Assess this cell for malaria.
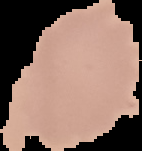
It is uninfected.

Summary:
  - Image type: cell region segmented out of the field of view; surrounding area masked to black
  - Preparation: thin blood smear
  - Image size: 142×151 pixels